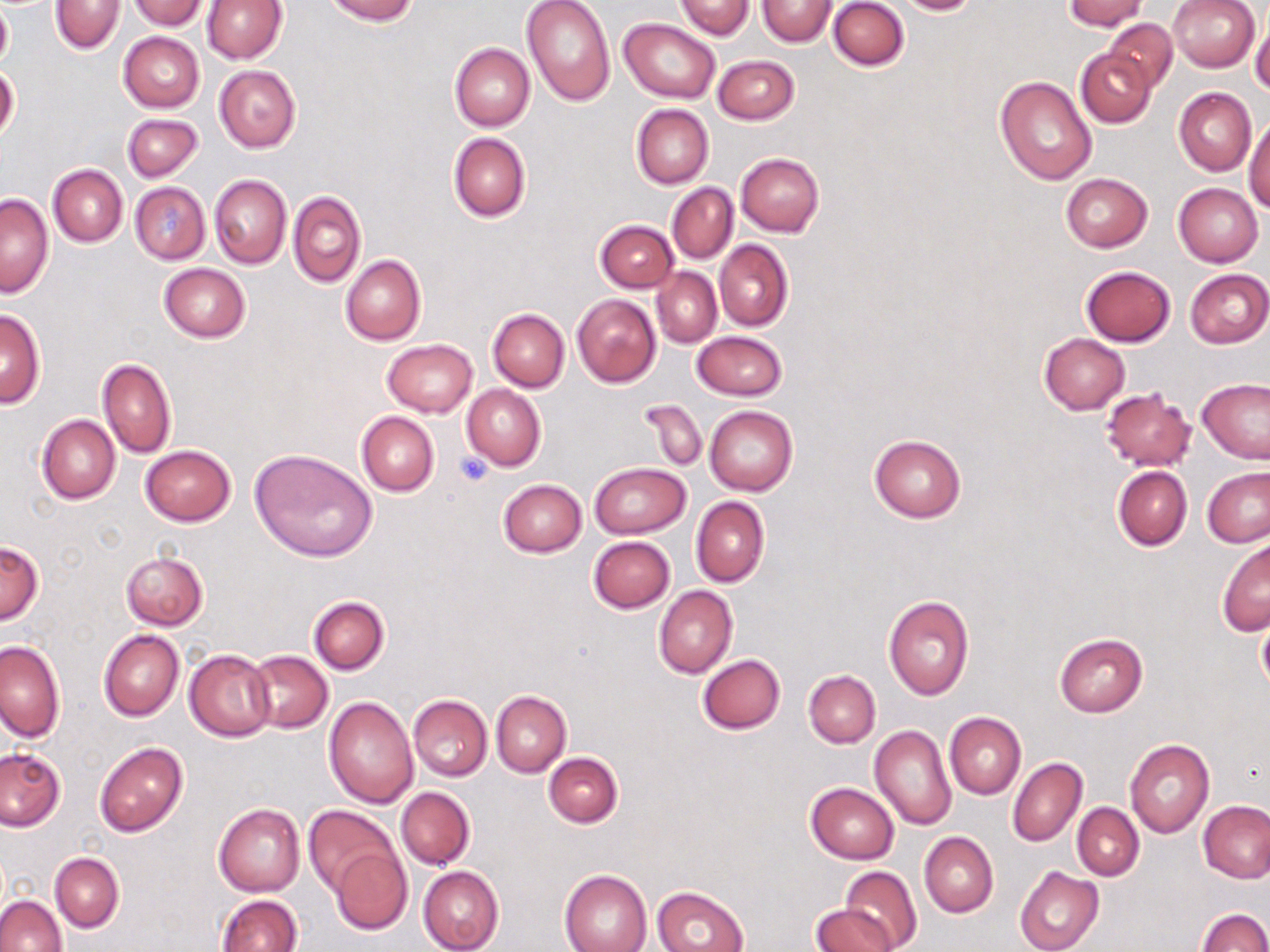

Approximate bounding boxes as (x1, y1, x2, y2) in pixels. Uninfected red blood cell locations: (0, 0, 11, 69), (129, 0, 206, 29), (324, 0, 418, 23), (520, 0, 615, 106), (756, 0, 836, 45), (828, 0, 908, 71), (895, 0, 982, 15), (1064, 0, 1146, 31), (1168, 0, 1261, 71), (50, 1, 124, 54), (201, 1, 285, 64), (675, 1, 754, 39), (621, 18, 720, 103), (1103, 18, 1178, 92), (1251, 18, 1270, 97), (119, 31, 204, 112), (450, 43, 535, 131), (1077, 50, 1155, 127), (712, 55, 800, 125), (214, 64, 301, 152), (0, 65, 19, 143), (994, 74, 1097, 185), (1174, 87, 1256, 176), (631, 104, 713, 188), (123, 112, 203, 181), (1245, 114, 1270, 212), (448, 132, 531, 222), (735, 152, 824, 236), (47, 164, 128, 247), (1059, 173, 1154, 252), (209, 175, 292, 268), (130, 182, 209, 263), (667, 182, 738, 264), (1173, 183, 1263, 267), (288, 191, 366, 288), (1, 194, 53, 298), (594, 219, 679, 292), (713, 239, 793, 332), (340, 255, 426, 345), (159, 263, 251, 342), (1080, 266, 1176, 346), (1184, 268, 1269, 348), (652, 269, 721, 347), (572, 294, 660, 388), (488, 308, 569, 391), (0, 310, 45, 407), (691, 331, 787, 401), (1039, 333, 1129, 414), (382, 339, 477, 417), (98, 358, 176, 459), (1198, 377, 1270, 463), (461, 384, 547, 470), (1100, 387, 1196, 471), (638, 397, 707, 470), (704, 404, 797, 496), (357, 411, 439, 497), (37, 414, 121, 504), (868, 434, 967, 523), (140, 444, 236, 526), (250, 449, 377, 561), (588, 462, 691, 539), (1113, 466, 1192, 550), (1203, 468, 1270, 547), (498, 479, 585, 557), (690, 496, 769, 588), (589, 536, 676, 613), (1217, 539, 1269, 636), (0, 540, 42, 624), (120, 550, 208, 630), (654, 585, 737, 678), (309, 595, 389, 675), (883, 596, 973, 699), (1255, 612, 1270, 697), (98, 630, 183, 721), (1054, 633, 1147, 717), (1, 640, 65, 742), (184, 649, 277, 741), (246, 650, 332, 732), (697, 654, 785, 734), (803, 670, 880, 748), (491, 690, 571, 776), (407, 694, 491, 782), (323, 695, 419, 809), (944, 712, 1026, 799), (869, 725, 957, 831), (1125, 740, 1214, 838), (94, 743, 188, 837), (0, 747, 67, 832), (543, 752, 622, 827), (1007, 757, 1086, 848), (805, 782, 899, 863), (396, 787, 474, 870), (1199, 801, 1270, 883), (1072, 803, 1143, 880), (213, 804, 305, 896), (304, 806, 400, 898), (919, 831, 998, 918), (331, 846, 410, 933), (50, 853, 123, 933), (419, 866, 504, 952), (839, 866, 922, 952), (1014, 866, 1104, 952), (560, 870, 652, 952), (652, 886, 748, 952), (0, 894, 67, 952), (216, 894, 301, 952), (810, 904, 898, 952), (1198, 908, 1270, 952). Platelet locations: (454, 452, 495, 487). Slide-level diagnosis: negative for blood parasites. Optical microscopy. Image is 1270×952 pixels. Single field of view. May-Grünwald-Giemsa-stained preparation. Thin blood film. Captured at 1000x magnification.